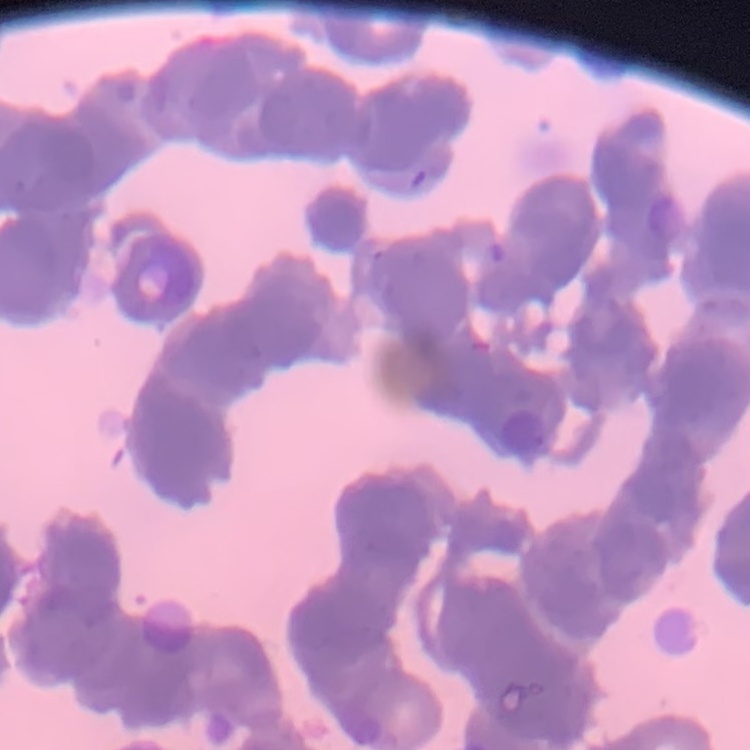

The red blood cells show rouleaux formation. Stained with either Field's or Giemsa. Square crop of a larger photomicrograph. Thin blood smear.